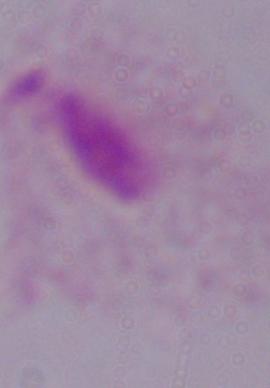 Micrograph. A trichomonad is seen. Captured at 1000x magnification.